Classify this cell by malaria status.
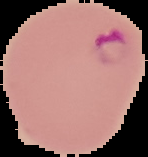
It is parasitized.

Summary:
  - Image type: segmented cell region with the area outside set to black
  - Preparation: thin blood film
  - Image size: 148×157 pixels